Identify the parasite.
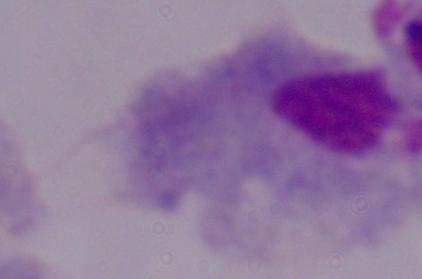

A trichomonad.

Micrograph. Captured at 1000x magnification.